Identify the parasite.
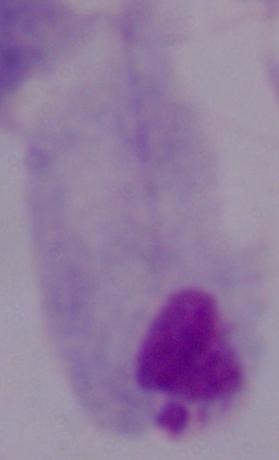
A trichomonad.

1000x magnification. Micrograph.